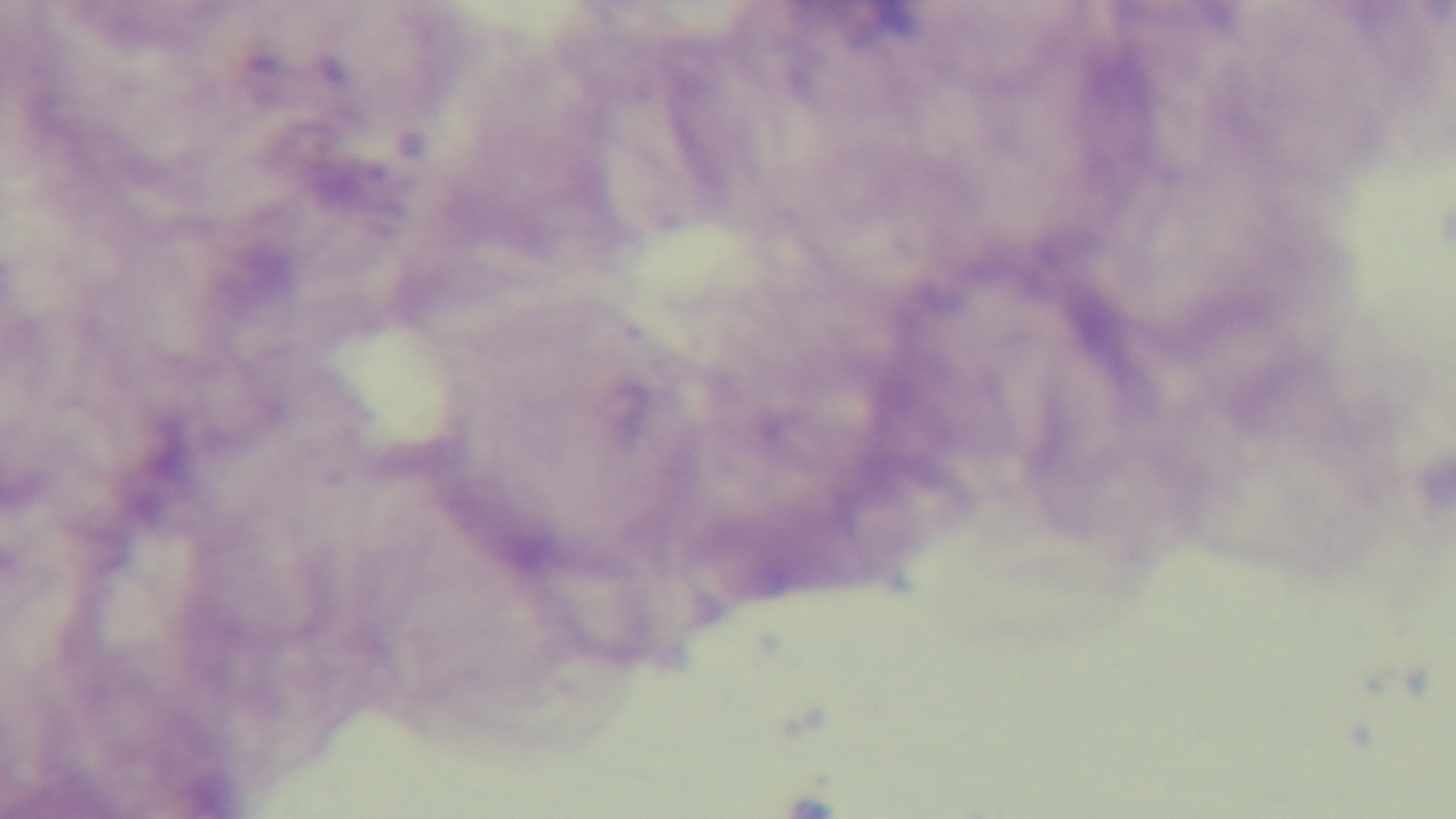
objective = 100x oil immersion
field of view = single
stain = Giemsa
preparation = thick
malaria status = uninfected
modality = light microscopy
capture = mounted 4K digital camera